Describe the morphology of the red blood cells.
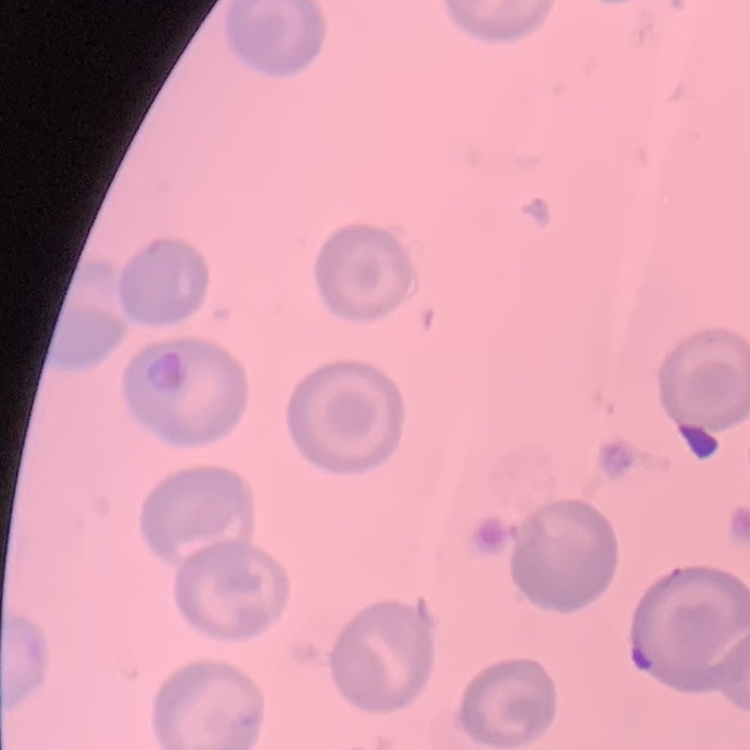

They show no rouleaux formation.

preparation = thin peripheral smear
stain = Field's or Giemsa
image type = one tile cut from a larger photomicrograph